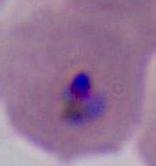 A Plasmodium parasite is seen. Photomicrograph. Captured at either 400x or 1000x magnification.